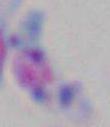

Toxoplasma gondii is shown. Photomicrograph. Captured at 1000x magnification.